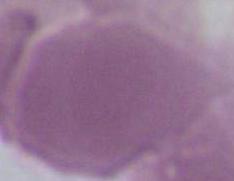 Micrograph. An erythrocyte is shown. Captured at 1000x magnification.